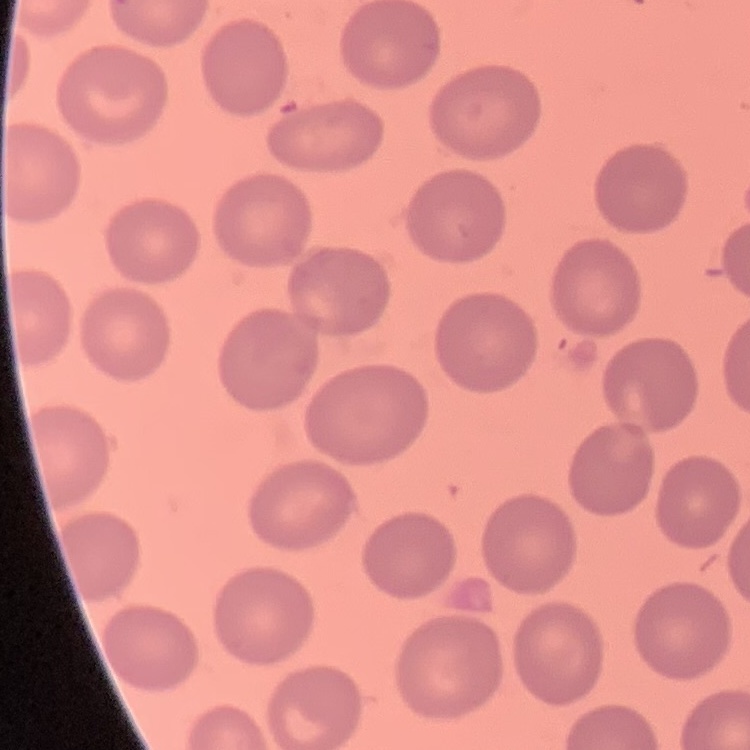

Summary:
  - Red blood cell morphology: no rouleaux formation
  - Preparation: thin peripheral smear
  - Image type: square crop of a larger photomicrograph
  - Stain: Field's or Giemsa